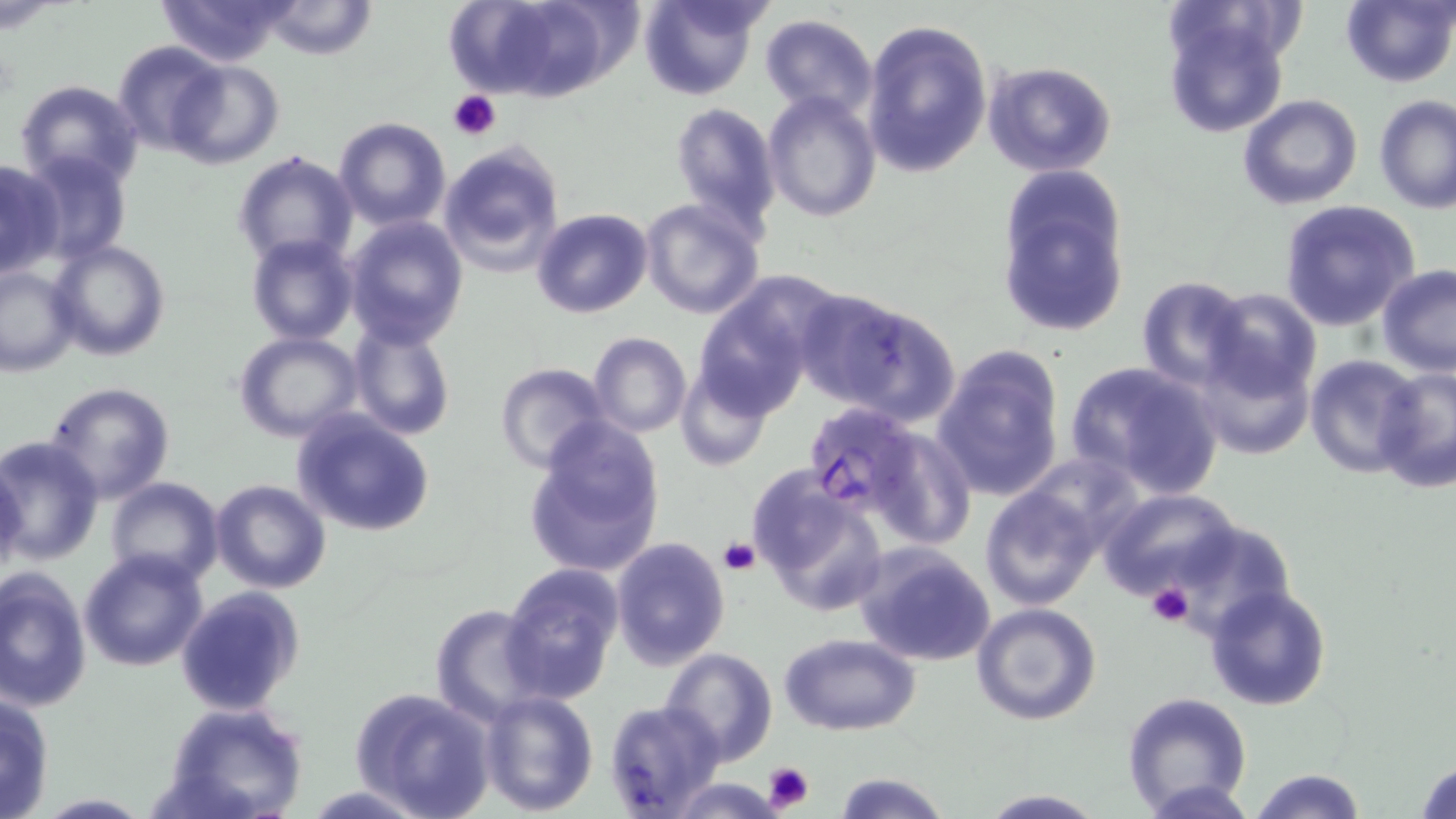

Summary:
  - Coordinate format: approximate bounding boxes as [x1, y1, x2, y2] in pixels
  - Uninfected red blood cell locations: [160, 0, 293, 66], [261, 0, 379, 61], [448, 0, 614, 104], [638, 0, 766, 102], [1339, 1, 1456, 88], [1161, 2, 1294, 140], [760, 13, 877, 120], [861, 18, 993, 177], [113, 41, 227, 157], [166, 59, 284, 169], [980, 61, 1119, 179], [14, 80, 144, 192], [763, 91, 882, 223], [1237, 93, 1364, 210], [1374, 95, 1455, 214], [668, 103, 782, 235], [334, 118, 452, 231], [435, 141, 565, 278], [231, 149, 358, 269], [19, 151, 132, 265], [0, 157, 66, 278], [994, 166, 1132, 339], [638, 198, 765, 319], [1279, 201, 1421, 330], [531, 208, 654, 318], [344, 213, 468, 346], [246, 234, 358, 343], [47, 237, 172, 361], [1376, 265, 1456, 377], [0, 266, 78, 377], [691, 276, 828, 419], [1136, 277, 1251, 390], [798, 287, 960, 423], [1199, 287, 1321, 407], [349, 321, 456, 441], [232, 331, 364, 445], [587, 332, 692, 439], [1189, 342, 1317, 460], [932, 346, 1066, 501], [1306, 355, 1424, 477], [1065, 362, 1224, 499], [494, 363, 614, 476], [674, 364, 775, 472], [1372, 366, 1456, 496], [44, 381, 176, 503], [291, 408, 438, 537], [523, 424, 665, 578], [866, 428, 974, 551], [0, 435, 104, 564], [0, 457, 28, 582], [748, 471, 887, 619], [105, 477, 225, 588], [210, 478, 332, 595], [980, 483, 1104, 611], [1098, 488, 1245, 607], [1164, 522, 1299, 634], [608, 535, 730, 670], [852, 542, 997, 667], [80, 549, 209, 672], [501, 562, 625, 702], [0, 567, 91, 713], [1203, 583, 1333, 713], [176, 586, 307, 716], [970, 602, 1102, 725], [431, 603, 551, 724], [780, 632, 921, 735], [660, 648, 778, 763], [349, 687, 497, 818], [478, 689, 599, 814], [1120, 691, 1253, 816], [0, 692, 56, 818], [603, 700, 726, 817], [161, 703, 309, 819], [1412, 757, 1456, 817], [1249, 767, 1366, 819], [832, 772, 953, 818], [665, 778, 789, 817], [297, 782, 441, 819], [974, 789, 1110, 819], [28, 793, 156, 819]
  - Platelet locations: [448, 90, 502, 141], [720, 536, 761, 577], [1146, 581, 1194, 628], [763, 761, 814, 813]
  - Plasmodium falciparum-infected red blood cell locations: [801, 402, 923, 519]
  - Slide-level diagnosis: Plasmodium falciparum
  - Image size: 1456×819 pixels
  - Stain: May-Grünwald-Giemsa
  - Field of view: one of a larger specimen
  - Modality: optical microscopy
  - Magnification: 1000x
  - Preparation: thin blood film